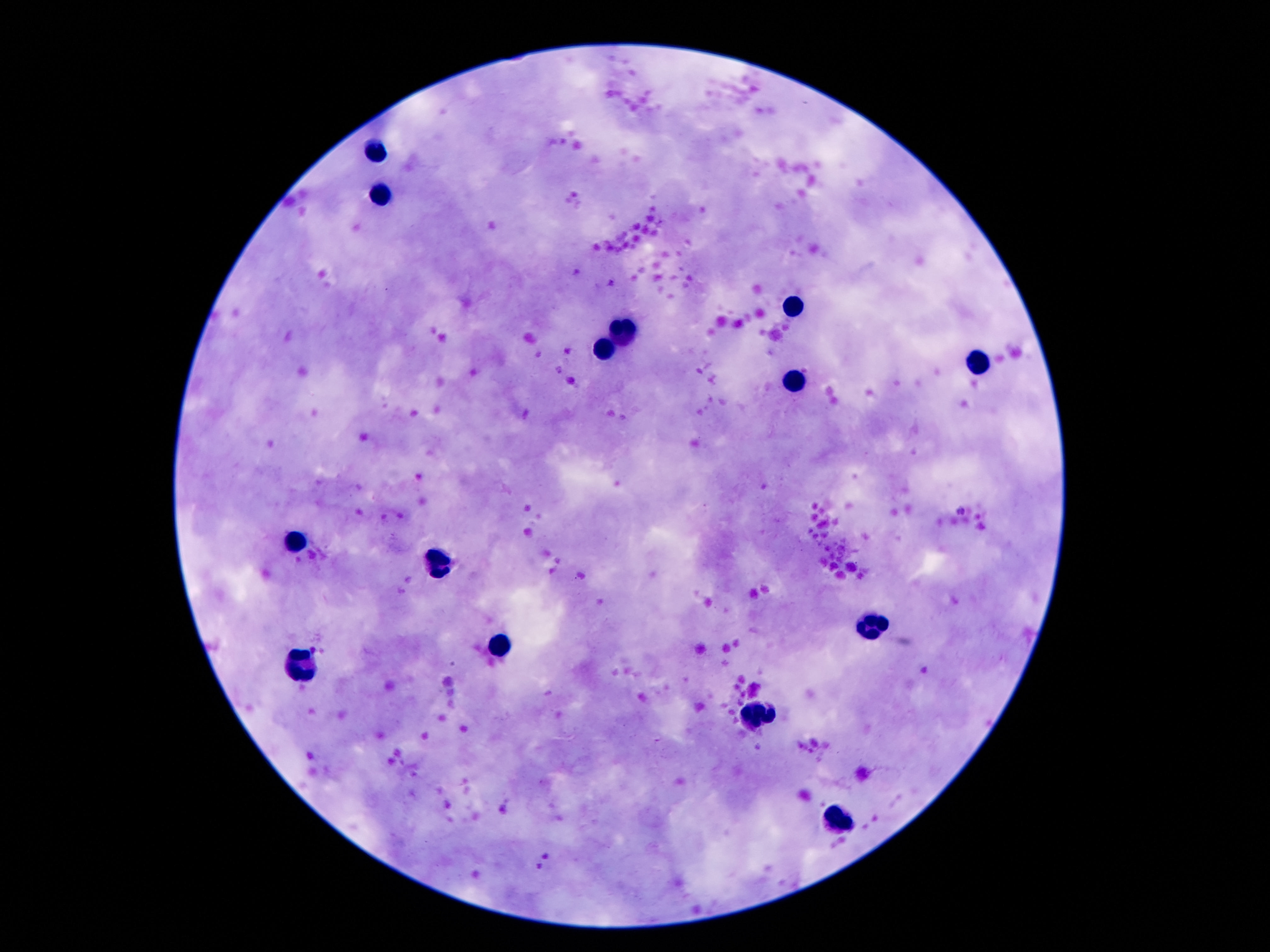
Approximate centers as {x, y} in pixels. Leukocyte locations: {374, 150}, {381, 193}, {797, 309}, {624, 329}, {602, 353}, {978, 364}, {799, 382}, {295, 540}, {441, 567}, {870, 628}, {505, 648}, {301, 666}, {753, 715}, {837, 821}. Giemsa stain. Single field of view. Image is 1270×952 pixels. Patient malaria status: negative. 100x magnification. Thick blood smear. Smartphone photograph taken through the microscope eyepiece.